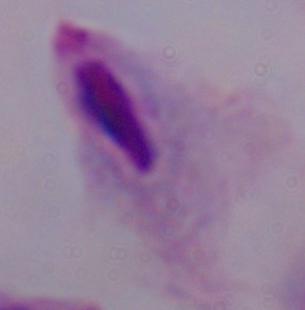

magnification = 1000x
identification = trichomonad
modality = micrograph